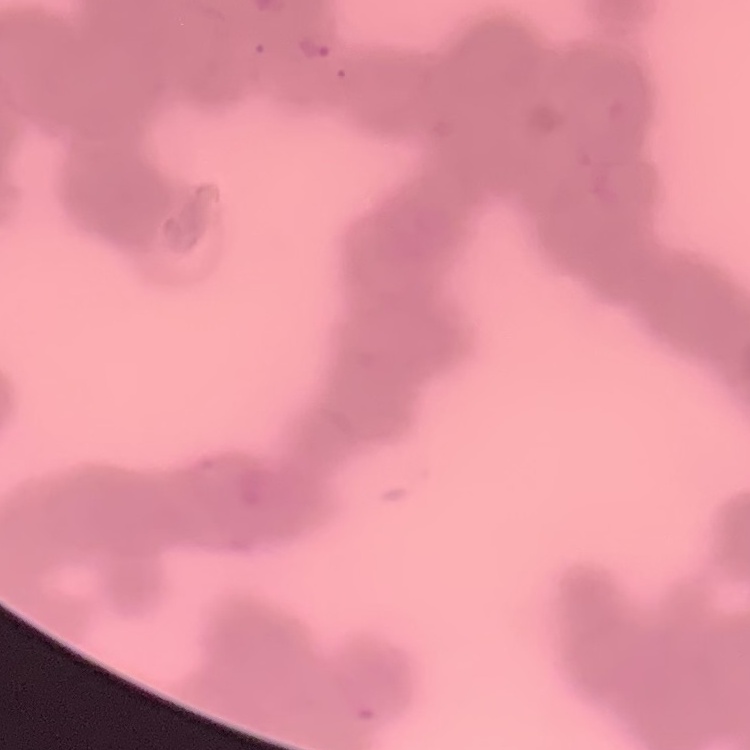

erythrocyte morphology = rouleaux formation
preparation = thin blood smear
image type = one tile cut from a larger photomicrograph
stain = Field's or Giemsa